Point out each malaria parasite.
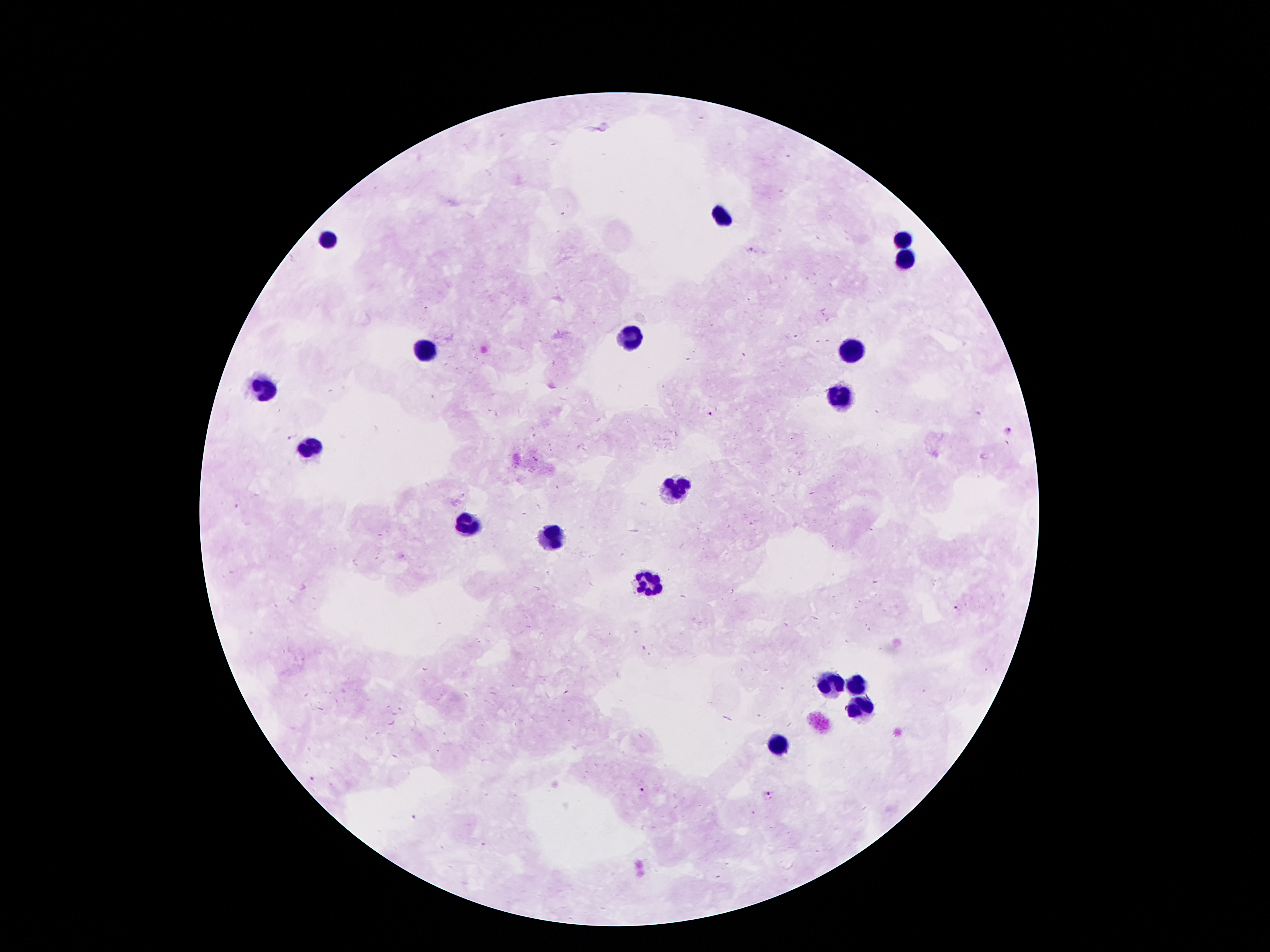
Approximate centers as [x, y] in pixels.
Malaria parasites: [751, 249], [710, 413], [1010, 431], [288, 439], [235, 505], [960, 607], [311, 779], [644, 792], [770, 795], [412, 815].

Leukocyte locations: [722, 216], [329, 243], [903, 243], [903, 260], [632, 335], [857, 346], [426, 348], [266, 390], [840, 396], [310, 447], [678, 486], [466, 524], [554, 537], [648, 583], [829, 684], [859, 684], [859, 707], [781, 745]. Thick peripheral-blood smear. 100x magnification. Image is 1270×952 pixels. Giemsa stain. Patient malaria status: infected with Plasmodium falciparum. Single field of view. Photographed through the microscope eyepiece with a smartphone camera.